Outline each blood parasite and name the species.
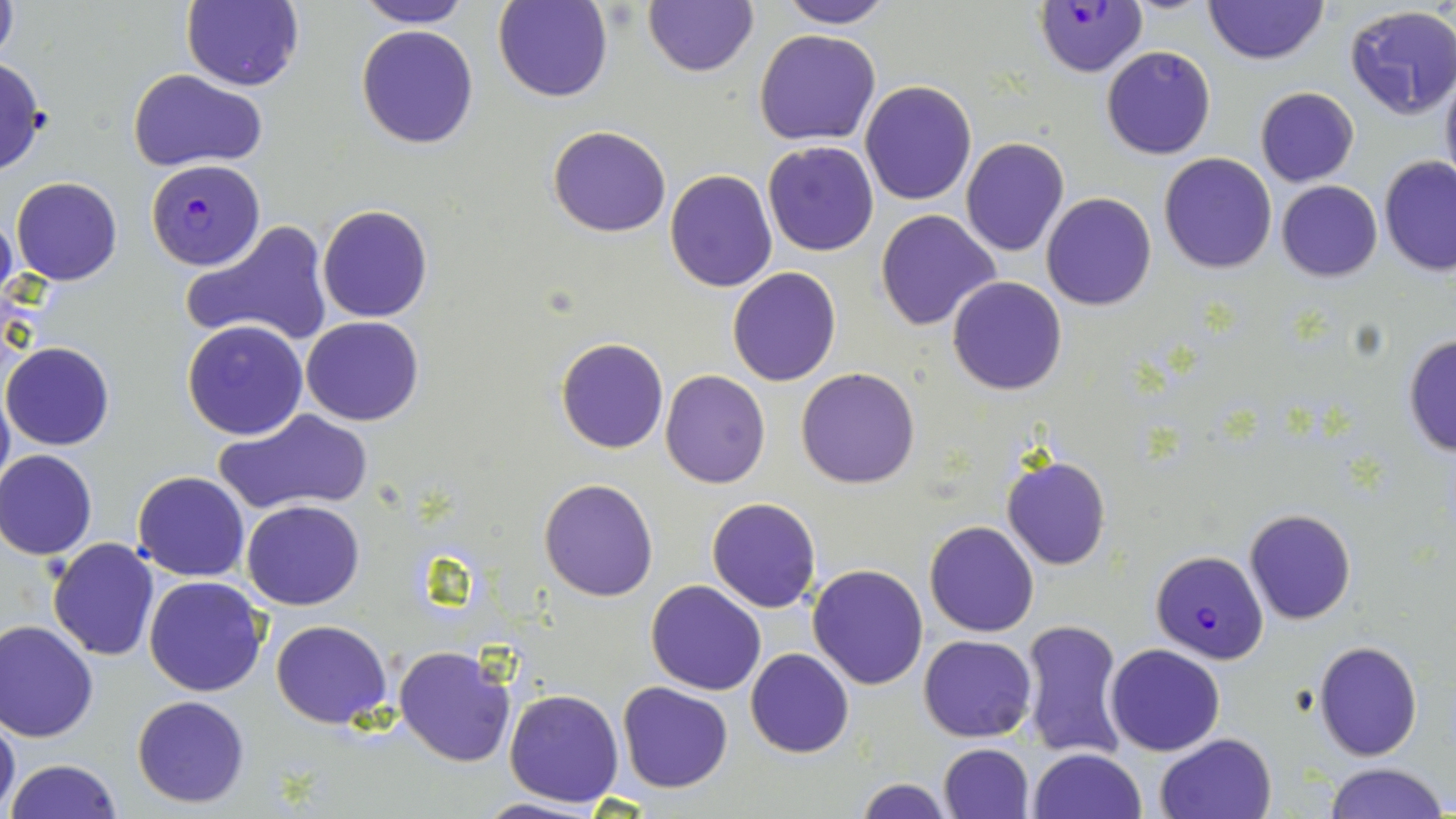
Approximate bounding boxes as named x1/y1/x2/y2 corners in pixels.
Plasmodium falciparum-infected red blood cells: (x1=1032, y1=1, x2=1150, y2=77), (x1=147, y1=158, x2=269, y2=273), (x1=1146, y1=546, x2=1272, y2=661).
No Plasmodium ovale, Plasmodium malariae, Plasmodium vivax, Babesia divergens, or Trypanosoma brucei observed.

Summary:
  - Uninfected red blood cell locations: (x1=0, y1=0, x2=20, y2=67), (x1=351, y1=0, x2=473, y2=27), (x1=495, y1=0, x2=613, y2=103), (x1=643, y1=0, x2=758, y2=78), (x1=777, y1=0, x2=895, y2=27), (x1=181, y1=1, x2=304, y2=91), (x1=1203, y1=1, x2=1329, y2=66), (x1=1345, y1=6, x2=1456, y2=119), (x1=356, y1=23, x2=481, y2=149), (x1=754, y1=28, x2=881, y2=146), (x1=1101, y1=45, x2=1217, y2=160), (x1=0, y1=56, x2=49, y2=175), (x1=129, y1=68, x2=266, y2=170), (x1=1439, y1=69, x2=1456, y2=197), (x1=860, y1=80, x2=977, y2=206), (x1=1254, y1=86, x2=1360, y2=186), (x1=547, y1=125, x2=671, y2=238), (x1=960, y1=137, x2=1069, y2=256), (x1=762, y1=140, x2=881, y2=256), (x1=1158, y1=153, x2=1278, y2=274), (x1=1380, y1=156, x2=1456, y2=277), (x1=664, y1=169, x2=778, y2=293), (x1=12, y1=178, x2=123, y2=286), (x1=1276, y1=180, x2=1382, y2=282), (x1=1042, y1=193, x2=1156, y2=310), (x1=316, y1=204, x2=434, y2=323), (x1=875, y1=208, x2=1001, y2=331), (x1=0, y1=209, x2=18, y2=311), (x1=181, y1=219, x2=334, y2=349), (x1=727, y1=267, x2=842, y2=386), (x1=946, y1=275, x2=1067, y2=396), (x1=300, y1=316, x2=424, y2=425), (x1=182, y1=319, x2=310, y2=441), (x1=1401, y1=333, x2=1456, y2=458), (x1=556, y1=337, x2=669, y2=454), (x1=2, y1=342, x2=114, y2=450), (x1=795, y1=367, x2=921, y2=490), (x1=660, y1=370, x2=771, y2=490), (x1=0, y1=380, x2=13, y2=503), (x1=214, y1=408, x2=376, y2=515), (x1=1, y1=450, x2=98, y2=559), (x1=1001, y1=458, x2=1111, y2=571), (x1=132, y1=470, x2=250, y2=581), (x1=539, y1=478, x2=659, y2=602), (x1=705, y1=498, x2=823, y2=611), (x1=242, y1=500, x2=365, y2=610), (x1=1243, y1=507, x2=1356, y2=624), (x1=925, y1=520, x2=1039, y2=637), (x1=47, y1=539, x2=160, y2=661), (x1=808, y1=563, x2=928, y2=689), (x1=144, y1=574, x2=268, y2=696), (x1=646, y1=580, x2=765, y2=695), (x1=1016, y1=618, x2=1131, y2=762), (x1=0, y1=619, x2=100, y2=742), (x1=271, y1=620, x2=393, y2=729), (x1=919, y1=635, x2=1036, y2=741), (x1=1314, y1=640, x2=1423, y2=760), (x1=1105, y1=643, x2=1225, y2=756), (x1=393, y1=644, x2=518, y2=766), (x1=745, y1=649, x2=854, y2=759), (x1=616, y1=682, x2=733, y2=793), (x1=504, y1=688, x2=625, y2=807), (x1=132, y1=695, x2=250, y2=807), (x1=0, y1=711, x2=21, y2=816), (x1=1155, y1=732, x2=1276, y2=819), (x1=938, y1=743, x2=1034, y2=819), (x1=1028, y1=748, x2=1146, y2=819), (x1=5, y1=758, x2=125, y2=818), (x1=1321, y1=762, x2=1449, y2=819), (x1=857, y1=777, x2=953, y2=819), (x1=472, y1=797, x2=609, y2=818)
  - Slide-level diagnosis: Plasmodium falciparum
  - Image size: 1456×819 pixels
  - Stain: May-Grünwald-Giemsa
  - Modality: optical microscopy
  - Field of view: one of a larger specimen
  - Magnification: 1000x
  - Preparation: thin blood film